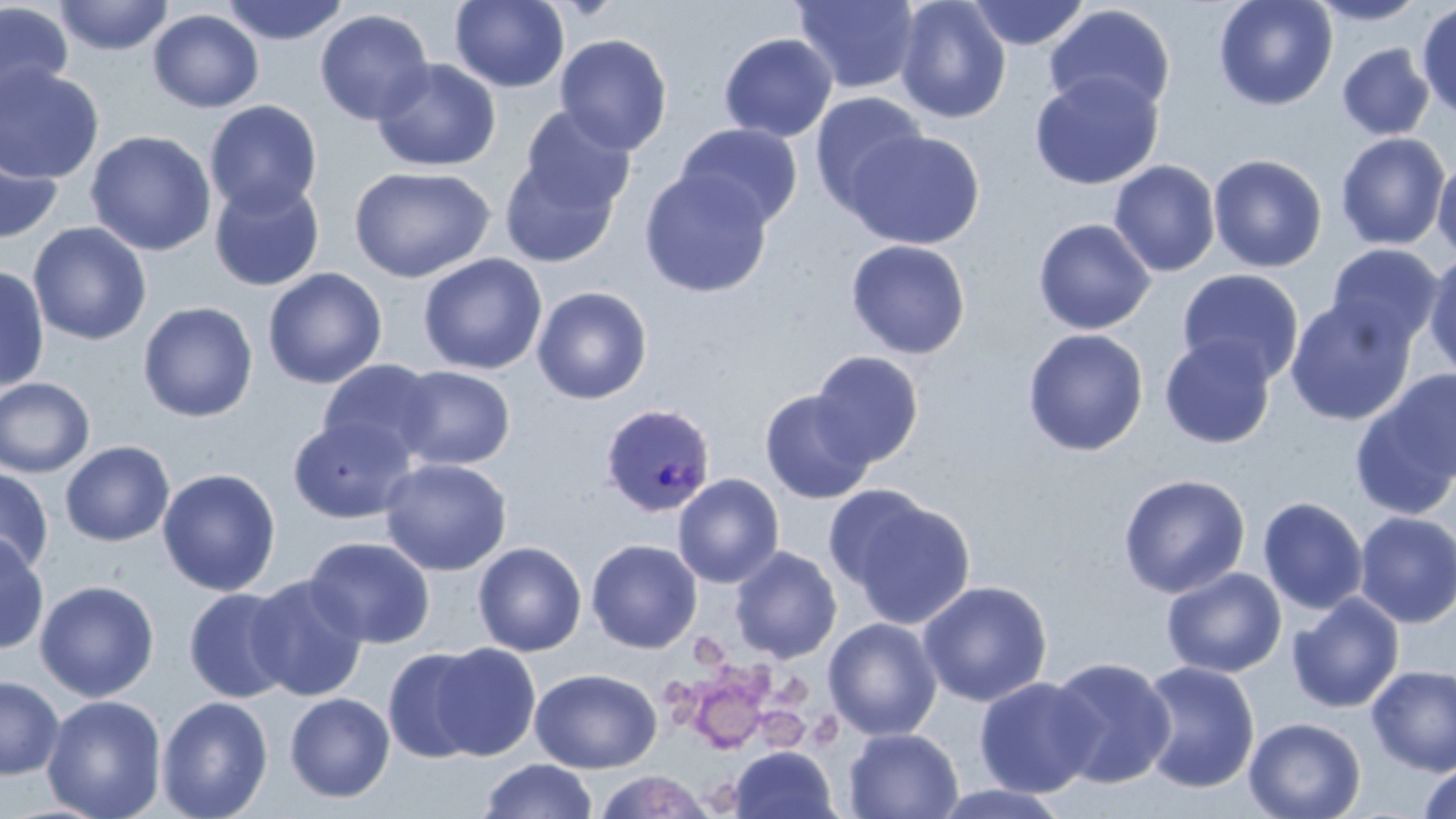

Summary:
  - Coordinate format: approximate bounding boxes as (x1, y1, x2, y2) in pixels
  - Platelet locations: (686, 635, 729, 672), (721, 662, 773, 699), (664, 676, 703, 725), (776, 676, 812, 710), (692, 686, 765, 754), (760, 708, 809, 748), (807, 710, 844, 751), (706, 779, 738, 813)
  - Plasmodium ovale-infected red blood cell locations: (599, 402, 717, 518)
  - Uninfected red blood cell locations: (54, 0, 174, 56), (220, 0, 349, 46), (450, 0, 569, 92), (792, 0, 922, 95), (895, 0, 1011, 123), (1213, 0, 1338, 111), (1308, 0, 1429, 26), (966, 1, 1090, 50), (0, 2, 74, 110), (1415, 3, 1456, 123), (1043, 4, 1175, 117), (148, 9, 264, 113), (314, 9, 434, 125), (554, 33, 673, 155), (718, 33, 838, 142), (1337, 43, 1435, 141), (372, 58, 501, 172), (0, 64, 105, 184), (1028, 71, 1164, 190), (809, 91, 928, 215), (204, 100, 322, 217), (516, 105, 637, 217), (674, 123, 803, 231), (844, 129, 985, 249), (85, 130, 217, 256), (1335, 132, 1450, 250), (0, 136, 63, 244), (500, 148, 626, 268), (1208, 153, 1328, 272), (1432, 157, 1456, 262), (1108, 160, 1221, 277), (348, 165, 495, 283), (639, 169, 773, 298), (209, 178, 325, 291), (1032, 218, 1156, 335), (28, 222, 152, 345), (845, 239, 971, 359), (1326, 243, 1443, 350), (1422, 251, 1456, 379), (418, 253, 547, 375), (0, 265, 50, 392), (262, 267, 387, 389), (1177, 268, 1304, 386), (532, 286, 652, 405), (1284, 297, 1416, 426), (137, 301, 258, 422), (1022, 328, 1149, 457), (1159, 335, 1276, 449), (809, 351, 924, 467), (318, 359, 441, 465), (393, 365, 516, 471), (1350, 372, 1455, 516), (0, 377, 95, 478), (760, 390, 876, 504), (287, 416, 417, 524), (59, 441, 175, 547), (379, 458, 512, 576), (0, 467, 54, 577), (157, 468, 281, 596), (672, 473, 784, 588), (1117, 473, 1251, 599), (831, 487, 976, 630), (1257, 496, 1368, 615), (1353, 512, 1456, 628), (0, 533, 49, 655), (304, 536, 436, 648), (586, 539, 702, 653), (472, 541, 587, 657), (729, 546, 842, 663), (1161, 567, 1287, 678), (245, 574, 369, 702), (34, 580, 159, 702), (917, 580, 1053, 707), (183, 588, 297, 703), (1287, 593, 1405, 713), (823, 617, 943, 740), (427, 642, 542, 761), (383, 647, 490, 762), (1047, 656, 1176, 789), (1137, 660, 1260, 793), (1367, 664, 1456, 775), (530, 668, 662, 773), (0, 676, 65, 780), (974, 676, 1102, 798), (284, 692, 395, 803), (41, 695, 167, 819), (156, 696, 274, 819), (1244, 716, 1366, 819), (843, 727, 964, 818), (729, 746, 838, 819), (481, 759, 597, 818), (1418, 763, 1456, 819), (594, 770, 714, 818), (930, 783, 1073, 818)
  - Slide-level diagnosis: Plasmodium ovale
  - Preparation: thin blood smear
  - Image size: 1456×819 pixels
  - Magnification: 1000x
  - Field of view: one of a larger specimen
  - Modality: light microscopy
  - Stain: May-Grünwald-Giemsa